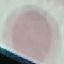

Malaria status: uninfected. Automatically extracted cell patch, resized to 64 × 64 pixels. Acquired by smartphone through the microscope eyepiece. Giemsa-stained preparation. Thin smear of blood.